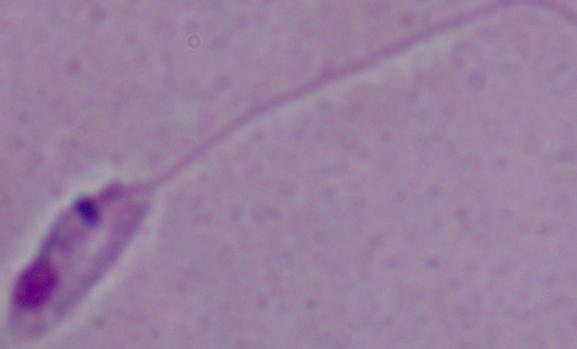

Micrograph. 1000x magnification. A Leishmania parasite is seen.